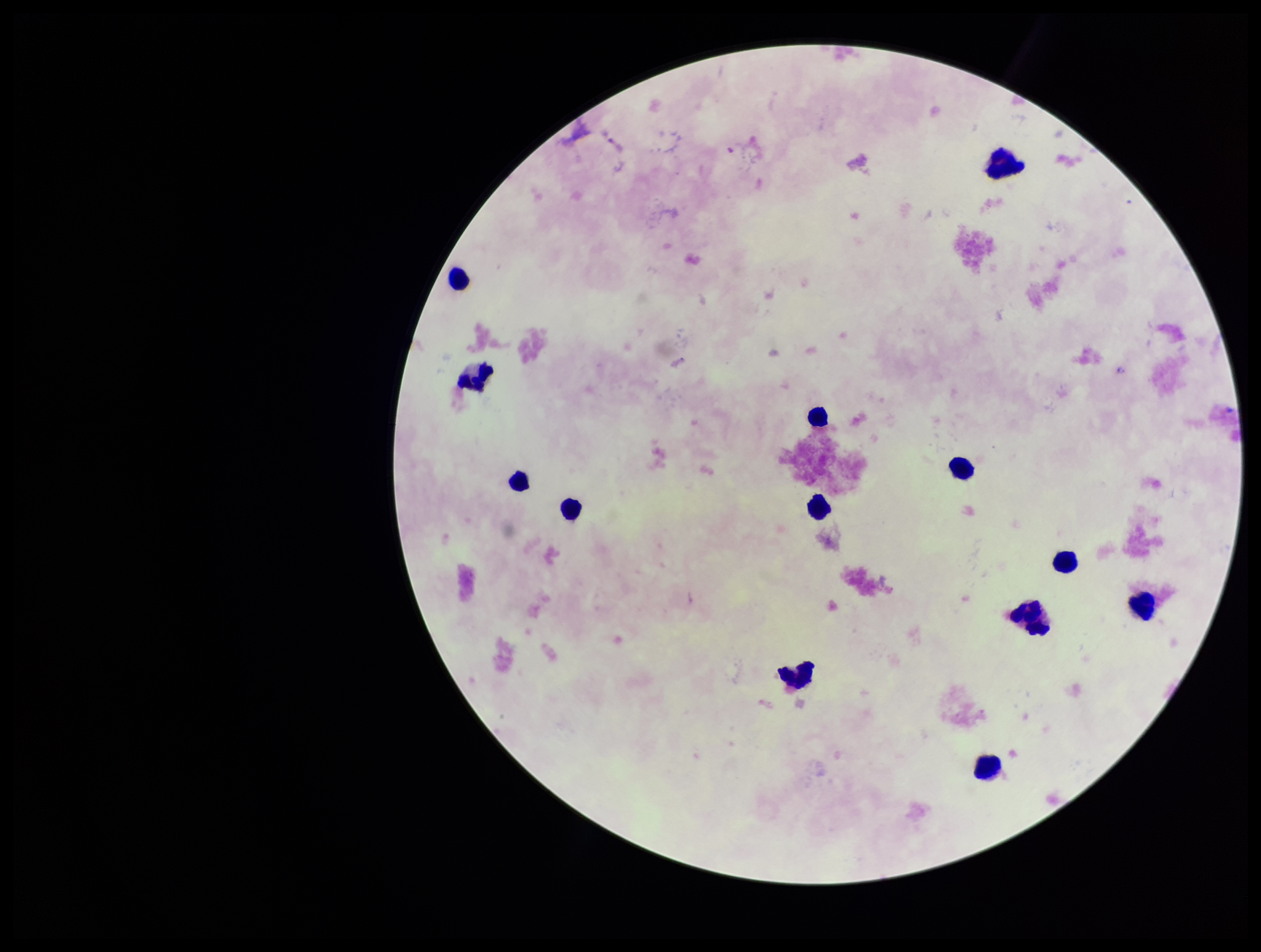
Leukocyte count: 13. Preparation: thick blood smear. Smartphone photograph taken through the eyepiece of a microscope. Giemsa stain. Image is 1261×952 pixels. Patient malaria status: negative. Plasmodium parasites: none seen. Parasite count: 0. One field from this slide.